State which parasite is depicted.
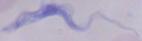
A trypanosome.

{
  "magnification": "1000x",
  "modality": "micrograph"
}